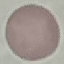

Malaria status: uninfected. Acquired by smartphone through the microscope eyepiece. Giemsa stain. Thin smear of blood. Cell patch, automatically extracted from a larger field of view and resized to 64 × 64 pixels.